Give the preparation type.
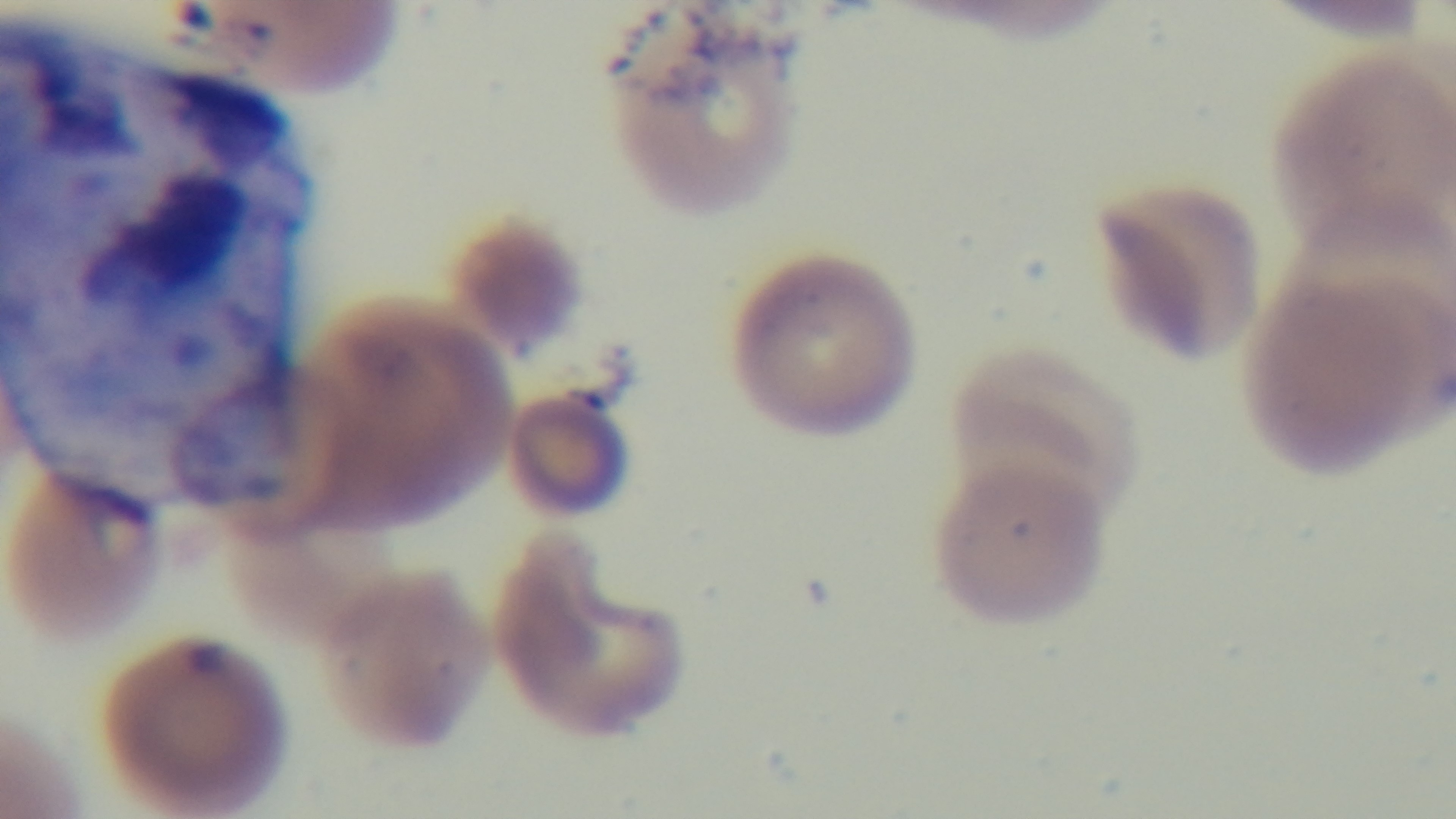

It is a thin blood film.

Single field of view. Giemsa-stained. Malaria status: infected. Light microscopy. Oil-immersion objective, 100x. Captured with a mounted 4K digital camera.